Give the extent of all Babesia divergens-infected red blood cells.
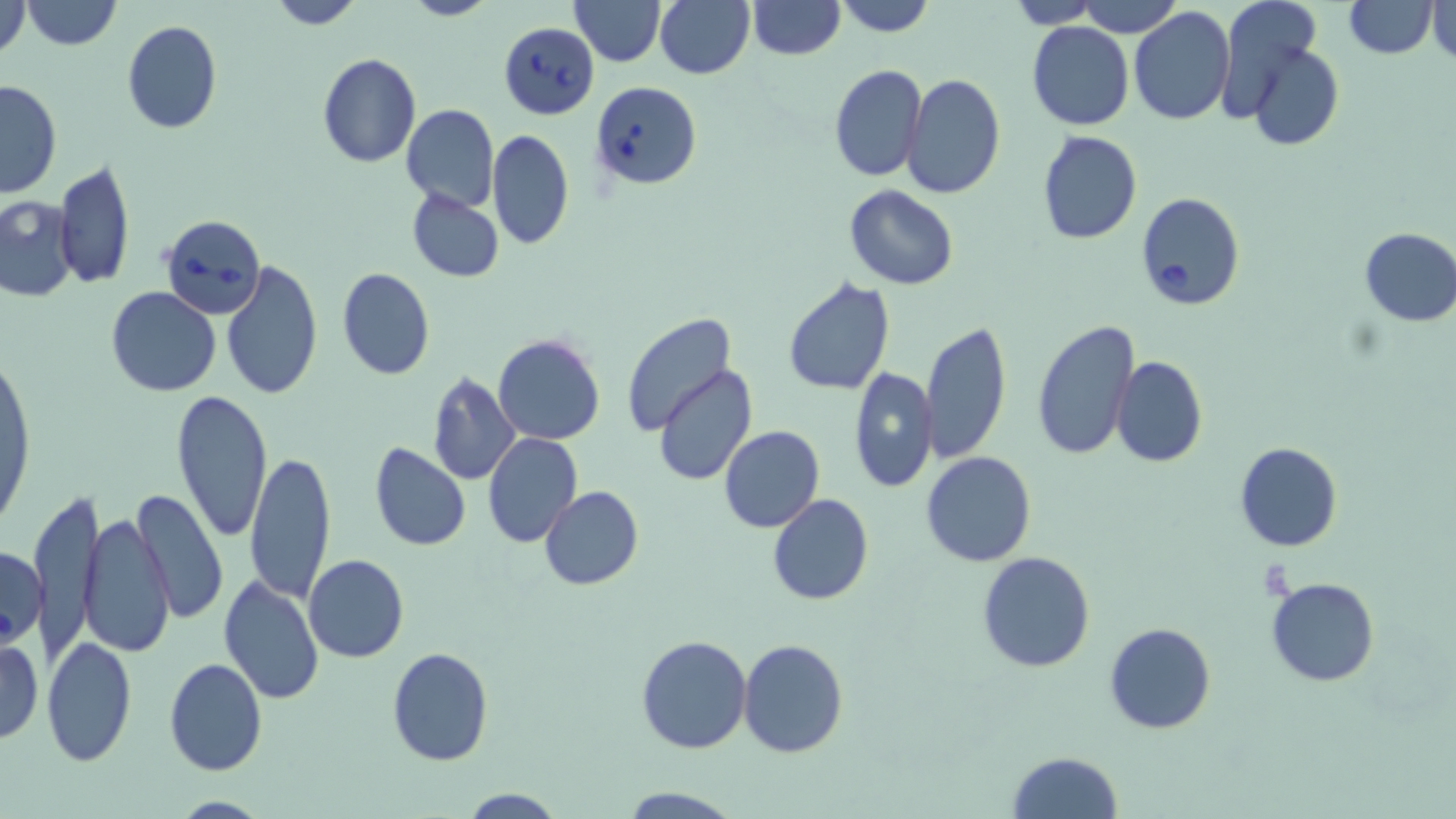
Approximate bounding boxes as [x1, y1, x2, y2] in pixels.
Babesia divergens-infected red blood cells: [499, 20, 601, 119], [590, 80, 702, 190], [1134, 192, 1245, 312], [161, 213, 266, 318].

Uninfected red blood cell locations: [0, 0, 31, 60], [22, 0, 122, 50], [265, 0, 364, 29], [400, 0, 494, 21], [570, 0, 664, 66], [655, 0, 754, 80], [746, 0, 845, 59], [834, 0, 936, 37], [1008, 0, 1105, 27], [1080, 0, 1183, 37], [1213, 0, 1326, 122], [1343, 0, 1437, 57], [1427, 1, 1454, 62], [1129, 6, 1237, 126], [120, 21, 223, 134], [1026, 21, 1135, 131], [1247, 41, 1343, 150], [317, 53, 421, 168], [829, 65, 926, 183], [902, 73, 1005, 198], [1, 79, 63, 199], [401, 104, 499, 212], [1037, 129, 1143, 245], [488, 130, 573, 250], [55, 159, 135, 289], [844, 185, 959, 289], [405, 188, 504, 283], [0, 195, 79, 302], [1358, 227, 1456, 326], [221, 259, 323, 401], [336, 267, 435, 381], [782, 276, 896, 396], [105, 287, 222, 397], [622, 313, 738, 437], [1031, 319, 1140, 459], [920, 320, 1012, 465], [494, 333, 604, 444], [1, 346, 35, 537], [1111, 357, 1206, 469], [653, 365, 757, 485], [848, 367, 938, 493], [427, 373, 521, 485], [171, 389, 274, 542], [719, 425, 824, 532], [482, 432, 583, 548], [368, 441, 471, 552], [1234, 443, 1343, 552], [245, 449, 335, 604], [921, 451, 1035, 567], [32, 486, 101, 657], [539, 486, 642, 590], [135, 489, 226, 629], [768, 494, 874, 606], [78, 511, 176, 657], [0, 543, 48, 653], [976, 551, 1096, 673], [304, 554, 409, 663], [218, 573, 325, 705], [1265, 577, 1380, 687], [1105, 623, 1216, 734], [0, 635, 43, 744], [636, 635, 752, 754], [43, 636, 136, 765], [738, 636, 848, 758], [386, 647, 494, 766], [163, 657, 268, 775], [1007, 750, 1124, 819], [618, 786, 742, 819], [461, 788, 565, 818], [170, 796, 270, 818]. Slide-level diagnosis: Babesia divergens. Thin blood film. Light microscopy. Captured at 1000x magnification. May-Grünwald-Giemsa-stained preparation. Image is 1456×819 pixels. One field of a larger specimen.